Assess the morphology of the red blood cells.
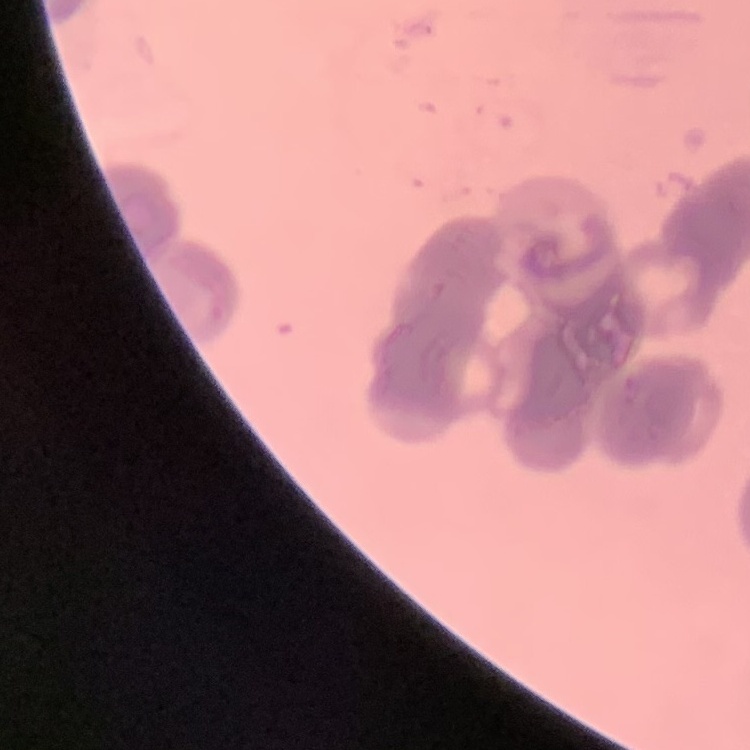
They show rouleaux formation.

stain: Field's or Giemsa
image_type: square crop of a larger photomicrograph
preparation: thin peripheral smear